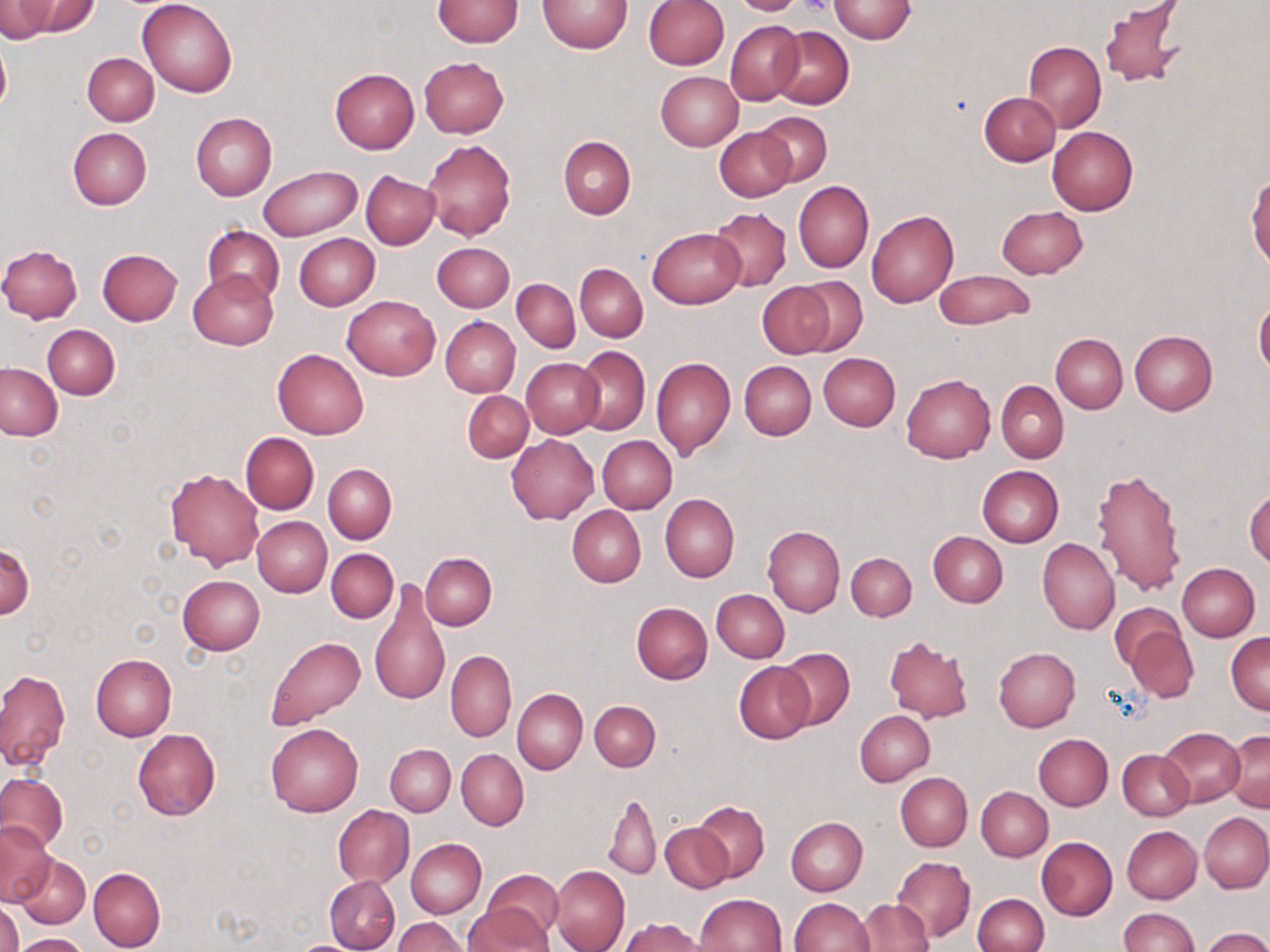

Summary:
  - Coordinate format: approximate bounding boxes as (x1, y1, x2, y2) in pixels
  - Platelet locations: (797, 0, 832, 17)
  - Uninfected red blood cell locations: (0, 0, 53, 42), (24, 0, 100, 36), (138, 0, 237, 97), (538, 0, 634, 53), (727, 0, 811, 15), (828, 0, 917, 44), (433, 1, 524, 47), (644, 1, 729, 70), (1099, 1, 1186, 90), (725, 21, 804, 104), (771, 25, 854, 109), (0, 37, 10, 120), (1024, 42, 1107, 131), (83, 53, 159, 126), (419, 56, 509, 137), (330, 68, 419, 155), (656, 71, 743, 150), (979, 92, 1060, 166), (190, 113, 277, 200), (756, 113, 832, 186), (714, 126, 795, 201), (1047, 127, 1138, 215), (67, 128, 152, 210), (558, 137, 636, 220), (422, 139, 516, 242), (259, 165, 360, 240), (361, 171, 439, 249), (1247, 173, 1269, 272), (793, 180, 874, 273), (996, 206, 1088, 277), (709, 207, 791, 291), (866, 208, 959, 308), (203, 227, 284, 306), (648, 227, 744, 308), (294, 233, 380, 310), (431, 242, 515, 313), (0, 244, 83, 323), (97, 248, 182, 325), (575, 264, 648, 342), (934, 270, 1034, 328), (189, 271, 278, 349), (793, 276, 869, 355), (512, 279, 580, 352), (758, 282, 835, 358), (343, 295, 440, 379), (1254, 297, 1270, 378), (440, 315, 520, 398), (43, 324, 119, 399), (1128, 331, 1217, 414), (1051, 333, 1127, 412), (575, 347, 650, 435), (273, 348, 369, 438), (818, 353, 900, 430), (651, 357, 735, 459), (521, 358, 603, 438), (740, 361, 815, 440), (0, 363, 64, 440), (901, 373, 995, 463), (997, 381, 1068, 462), (463, 390, 533, 462), (240, 432, 319, 514), (507, 433, 598, 524), (597, 435, 677, 513), (323, 463, 396, 543), (977, 466, 1063, 546), (1090, 467, 1186, 597), (165, 468, 265, 570), (1245, 488, 1270, 568), (661, 495, 739, 581), (567, 504, 646, 587), (253, 516, 332, 597), (763, 525, 844, 617), (928, 531, 1007, 607), (1038, 538, 1118, 634), (1, 542, 34, 619), (326, 548, 398, 623), (846, 552, 917, 621), (421, 553, 496, 629), (1177, 562, 1259, 641), (177, 575, 265, 654), (369, 581, 450, 708), (711, 589, 790, 662), (631, 601, 712, 684), (1110, 602, 1187, 675), (1124, 625, 1199, 704), (1226, 631, 1269, 714), (884, 635, 974, 722), (265, 636, 365, 730), (776, 647, 855, 729), (994, 647, 1080, 731), (446, 650, 516, 741), (90, 653, 176, 741), (734, 661, 815, 744), (0, 669, 70, 771), (513, 688, 587, 775), (589, 700, 660, 771), (854, 710, 934, 786), (266, 722, 363, 816), (1159, 726, 1246, 806), (133, 729, 220, 820), (1225, 729, 1270, 812), (1033, 733, 1113, 810), (386, 744, 454, 816), (457, 749, 528, 829), (1117, 750, 1194, 820), (0, 772, 67, 851), (895, 773, 971, 851), (976, 786, 1052, 860), (604, 791, 661, 881), (693, 801, 768, 883), (333, 805, 413, 887), (1199, 812, 1270, 893), (786, 816, 867, 895), (1, 822, 54, 905), (661, 822, 732, 893), (1122, 825, 1202, 904), (1036, 837, 1117, 921), (407, 839, 486, 917), (413, 846, 544, 931), (14, 853, 90, 929), (892, 856, 975, 942), (551, 865, 630, 952), (90, 867, 165, 952), (478, 869, 564, 948), (325, 876, 399, 952), (696, 893, 786, 952), (973, 894, 1048, 952), (789, 898, 874, 951), (857, 898, 932, 951), (1, 901, 23, 952), (463, 903, 555, 952), (1118, 907, 1198, 952), (393, 917, 467, 952), (620, 918, 707, 952), (1201, 927, 1270, 952), (10, 933, 92, 952)
  - Slide-level diagnosis: negative for blood parasites
  - Field of view: single
  - Image size: 1270×952 pixels
  - Preparation: thin blood film
  - Stain: May-Grünwald-Giemsa
  - Magnification: 1000x
  - Modality: optical microscopy